Locate every Plasmodium parasite by life-cycle stage, and every leukocyte.
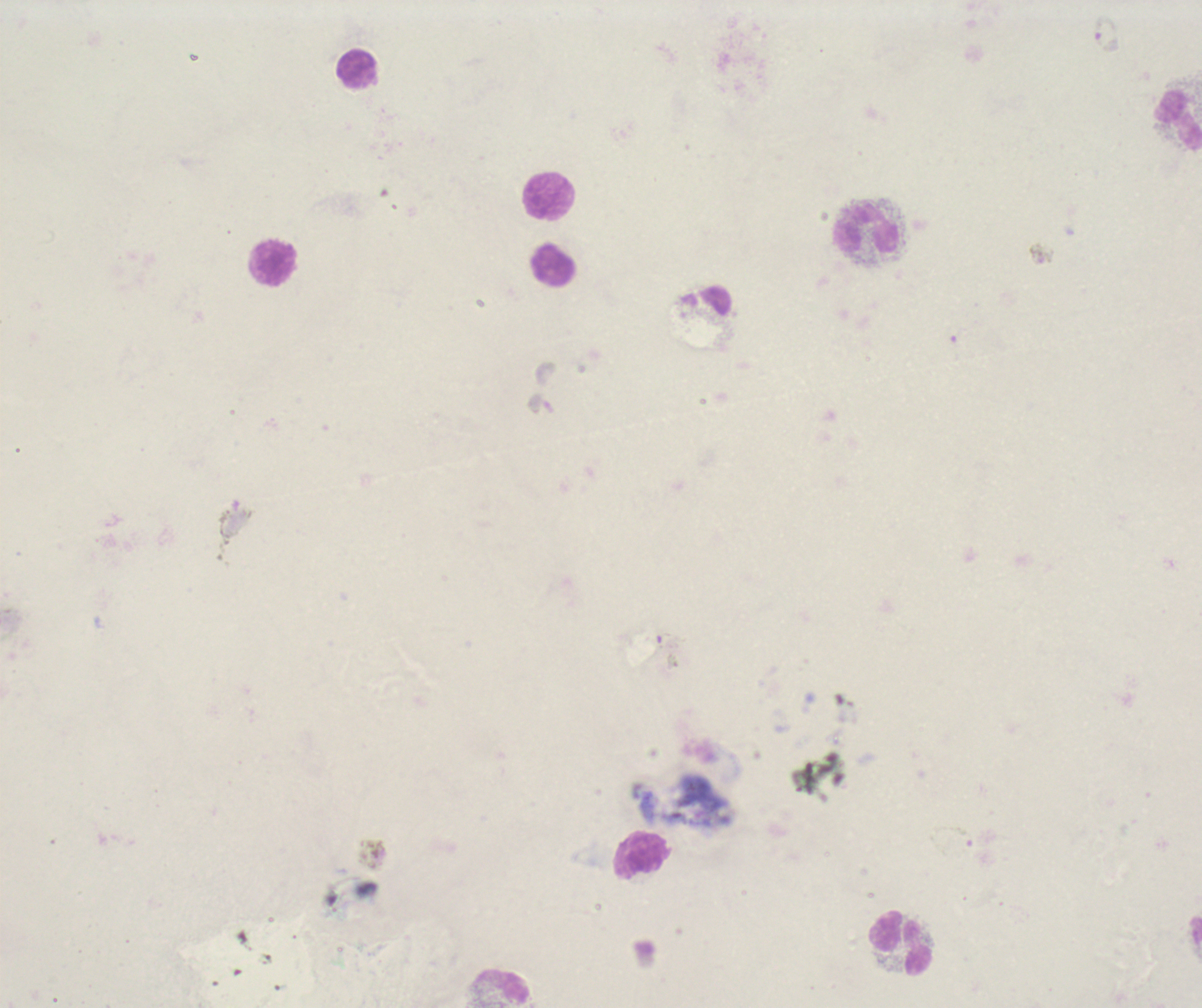
Approximate centers as (x, y) in pixels.
Gametocytes: (1106, 34), (1042, 255).
No trophozoite or schizont forms observed.
Leukocytes: (356, 68), (1177, 118), (551, 196), (867, 228), (275, 263), (554, 264), (640, 855), (903, 944), (502, 987).

Summary:
  - Background quality: poor
  - Magnification: 100x
  - Stain: Romanowsky
  - Image size: 1202×1008 pixels
  - Context: previously used in an actual diagnosis
  - Coloration quality: bad
  - Preparation: thick blood film
  - Field of view: single